Name the parasite shown.
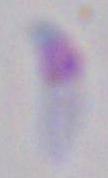

This is Toxoplasma gondii.

Photomicrograph. Captured at 1000x magnification.